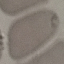
result: no malaria parasites seen
preparation: thin blood smear
image_type: cell patch, automatically extracted from a larger field of view and resized to 64 × 64 pixels
capture: smartphone through the microscope eyepiece
stain: Giemsa